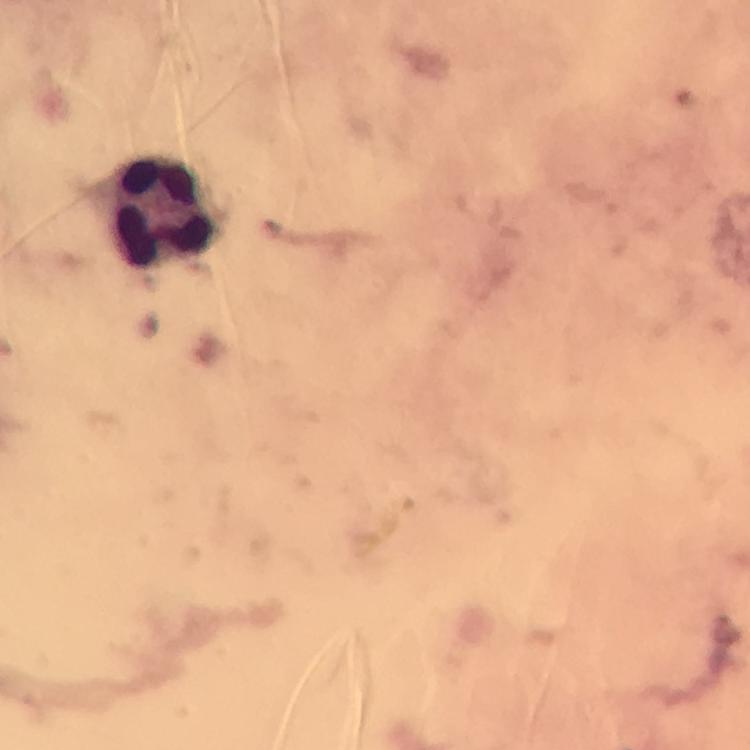

Approximate object centers, in pixels from the top-left corner.
Summary:
  - Leukocyte locations: (x=163, y=214)
  - Capture: smartphone photograph through a microscope
  - Magnification: 100x
  - Preparation: thick blood film
  - Immersion oil: applied
  - Context: from a diagnostic examination for malaria
  - Cropped from: a single field of view
  - Plasmodium parasites: none seen
  - Image size: 750×750 pixels
  - Stain: Giemsa